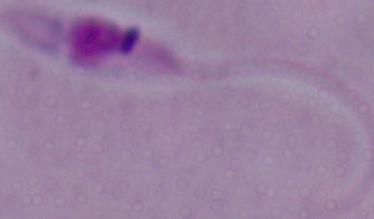
modality = micrograph
identification = Leishmania
magnification = 1000x